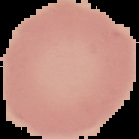 From a thin blood film. Image is 139×139 pixels. Malaria status: uninfected. Cell region segmented out of the field of view; the surrounding area is masked to black.